Describe the morphology of the erythrocytes.
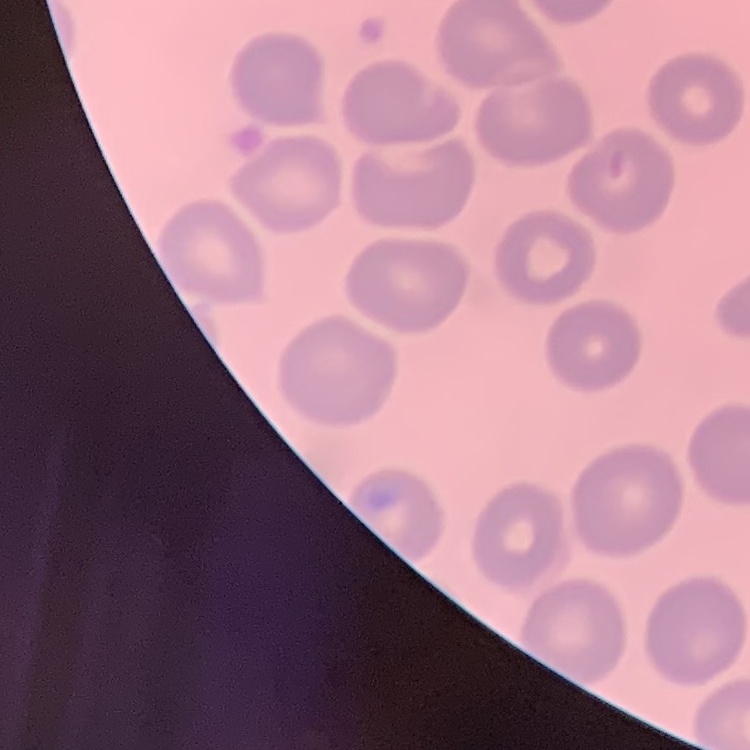
No rouleaux formation.

Field's or Giemsa stain. Square crop of a larger photomicrograph. Thin blood smear.